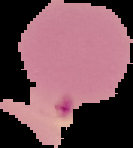 From a thin blood smear. Image is 133×148 pixels. Malaria status: parasitized. Cell region segmented out of the field of view; the surrounding area is masked to black.